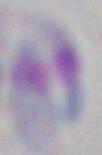

Summary:
  - Modality: micrograph
  - Magnification: 1000x
  - Identification: Toxoplasma gondii